Name the cell type shown.
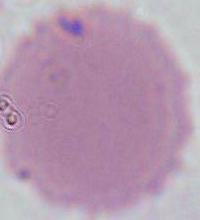

An erythrocyte.

modality = photomicrograph
magnification = 1000x